Locate and identify every blood parasite.
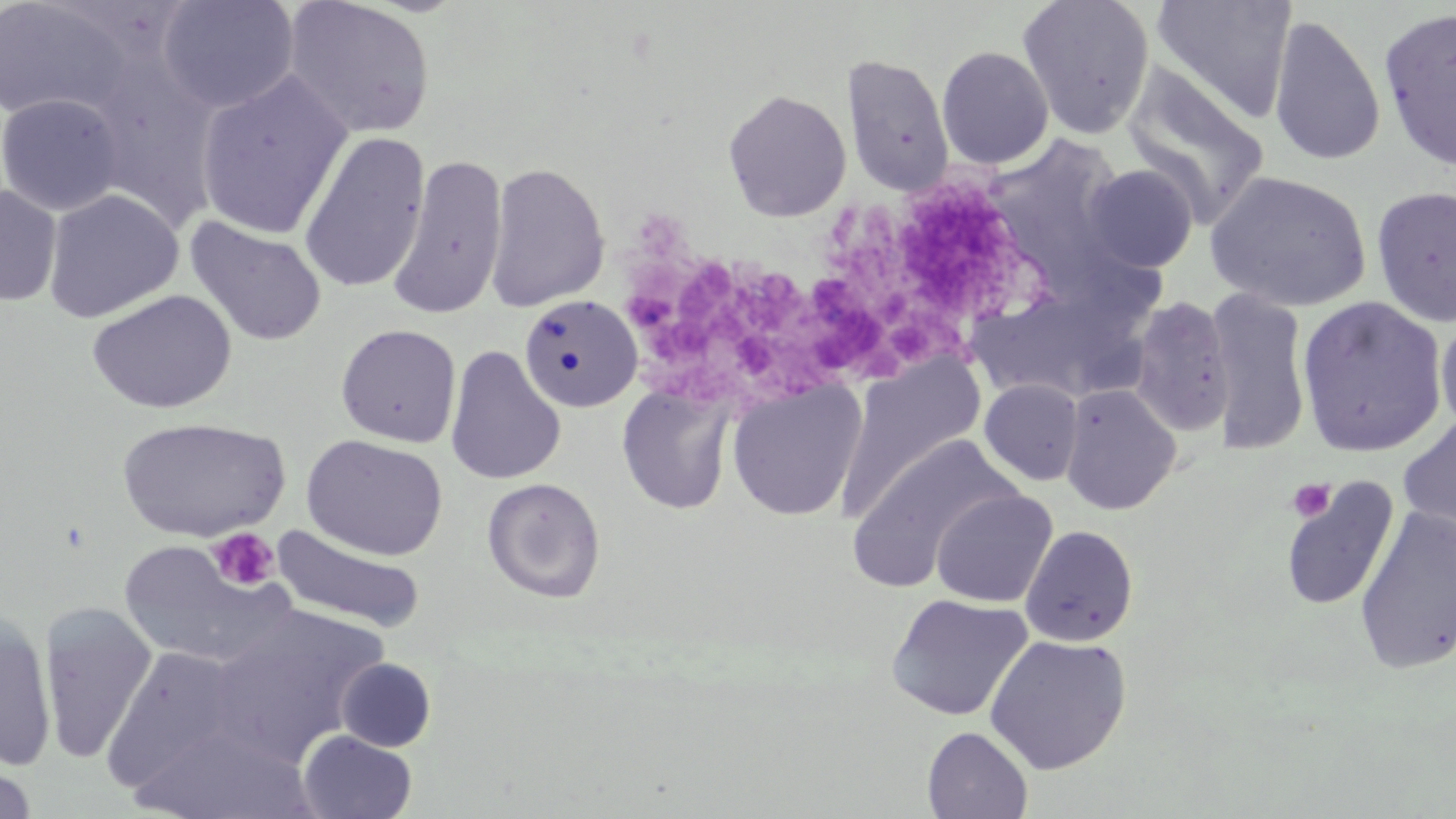
No blood parasites seen.

Summary:
  - Coordinate format: approximate bounding boxes as (x1, y1, x2, y2) in pixels
  - Uninfected red blood cell locations: (156, 0, 299, 114), (282, 0, 436, 141), (1017, 0, 1155, 141), (1149, 0, 1297, 124), (0, 1, 136, 123), (1379, 7, 1456, 171), (1268, 13, 1386, 167), (936, 46, 1054, 170), (841, 53, 955, 197), (79, 62, 223, 231), (1121, 65, 1271, 227), (194, 70, 354, 241), (722, 88, 851, 222), (0, 93, 124, 216), (297, 131, 431, 296), (389, 155, 508, 320), (484, 161, 610, 313), (1085, 165, 1198, 272), (1205, 170, 1372, 312), (0, 184, 61, 307), (1371, 187, 1456, 326), (43, 188, 184, 323), (185, 217, 328, 347), (1205, 288, 1312, 457), (86, 289, 236, 414), (518, 295, 642, 414), (1295, 296, 1447, 458), (1128, 297, 1235, 437), (1435, 311, 1456, 437), (336, 324, 462, 448), (445, 345, 566, 485), (835, 354, 986, 523), (726, 379, 867, 522), (979, 379, 1084, 486), (617, 382, 738, 515), (1060, 383, 1182, 516), (1397, 414, 1456, 548), (117, 416, 290, 541), (846, 433, 1024, 591), (300, 434, 449, 561), (482, 478, 606, 603), (1280, 479, 1399, 611), (931, 489, 1057, 607), (1355, 506, 1456, 675), (270, 523, 426, 635), (1020, 525, 1139, 647), (116, 540, 298, 670), (886, 593, 1033, 723), (38, 602, 158, 766), (204, 603, 389, 766), (0, 611, 57, 771), (984, 634, 1132, 775), (103, 645, 248, 791), (336, 658, 436, 752), (131, 724, 319, 819), (922, 726, 1034, 818), (296, 730, 418, 818), (0, 760, 38, 819)
  - Platelet locations: (1287, 478, 1335, 522), (207, 527, 281, 592)
  - Slide-level diagnosis: no evidence of blood parasites
  - Magnification: 1000x
  - Image size: 1456×819 pixels
  - Field of view: one of a larger specimen
  - Preparation: thin blood film
  - Stain: May-Grünwald-Giemsa
  - Modality: light microscopy